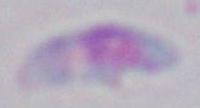 Captured at 1000x magnification. Micrograph. Toxoplasma gondii is shown.